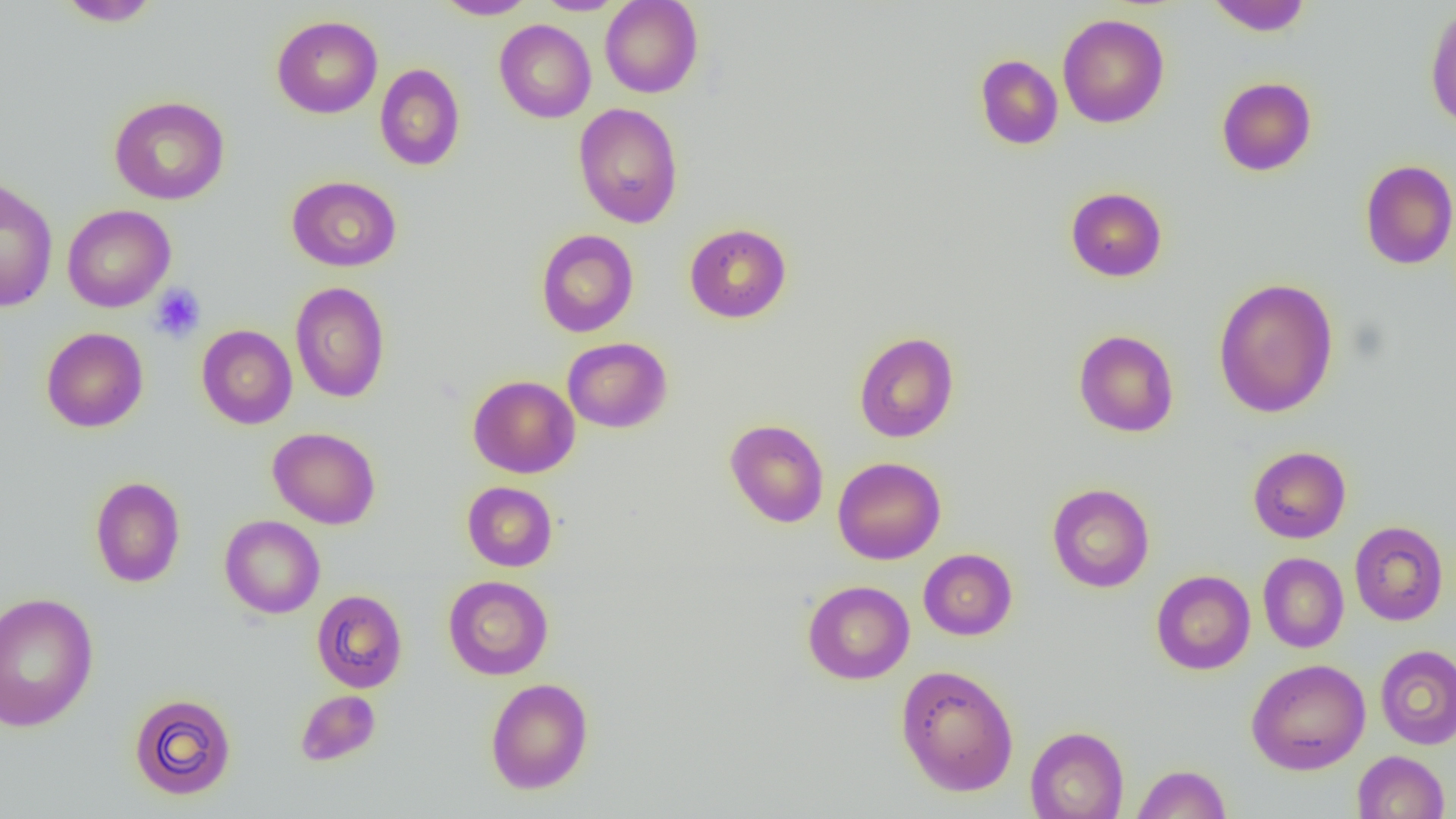
Approximate bounding boxes as (x1,y1)-(x2,y2) corner pairs in pixels. Platelet locations: (149,284)-(206,343). Uninfected red blood cell locations: (56,0)-(163,27), (433,0)-(536,19), (533,0)-(627,15), (600,0)-(703,98), (1206,0)-(1312,36), (1424,4)-(1456,131), (1057,13)-(1170,128), (271,15)-(383,118), (495,19)-(596,123), (975,54)-(1063,149), (375,63)-(466,171), (1216,76)-(1317,176), (108,95)-(230,205), (573,103)-(684,228), (1360,159)-(1456,270), (286,176)-(401,272), (1,177)-(58,312), (1066,187)-(1167,281), (62,204)-(176,312), (684,223)-(792,323), (536,229)-(639,337), (1212,277)-(1340,419), (290,282)-(390,403), (196,324)-(298,429), (41,327)-(149,432), (1074,330)-(1179,437), (854,331)-(959,443), (563,337)-(672,432), (468,375)-(579,478), (725,419)-(829,528), (268,427)-(381,529), (1248,446)-(1351,543), (833,457)-(946,565), (90,476)-(185,588), (462,481)-(558,571), (1047,483)-(1155,592), (220,515)-(325,618), (1349,521)-(1449,626), (918,549)-(1017,640), (1258,552)-(1349,653), (1151,570)-(1255,675), (443,575)-(554,680), (803,580)-(915,684), (311,589)-(408,693), (0,590)-(99,733), (1375,644)-(1456,749), (1246,658)-(1370,775), (895,663)-(1019,797), (485,678)-(594,794), (295,690)-(381,766), (128,693)-(237,800), (1025,726)-(1129,819), (1352,750)-(1451,819), (1131,764)-(1232,818). Slide-level diagnosis: no evidence of blood parasites. Image is 1456×819 pixels. Optical microscopy. 1000x magnification. Thin blood smear. Single field of view.